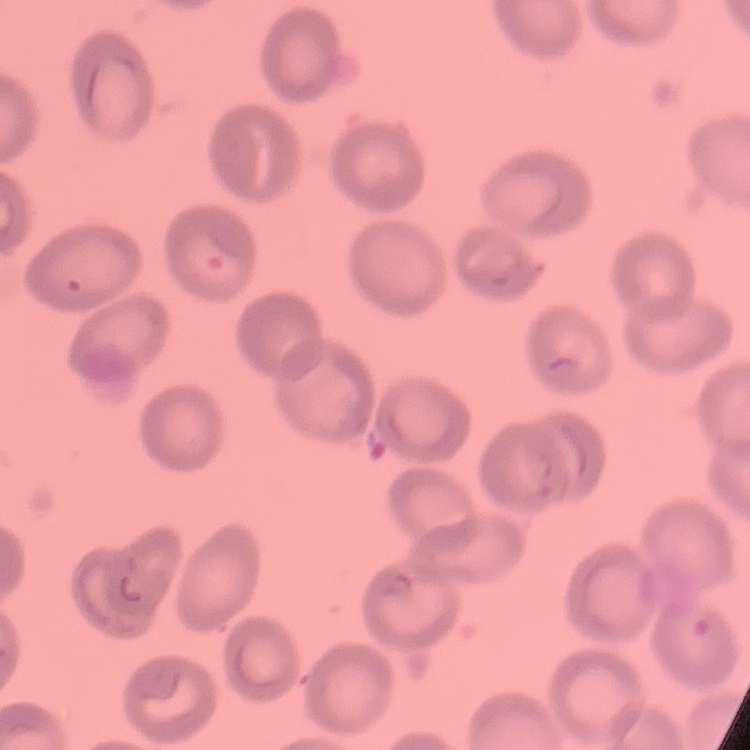 The erythrocytes exhibit no rouleaux formation. Stained with either Field's or Giemsa. Thin blood film. One tile cut from a larger photomicrograph.